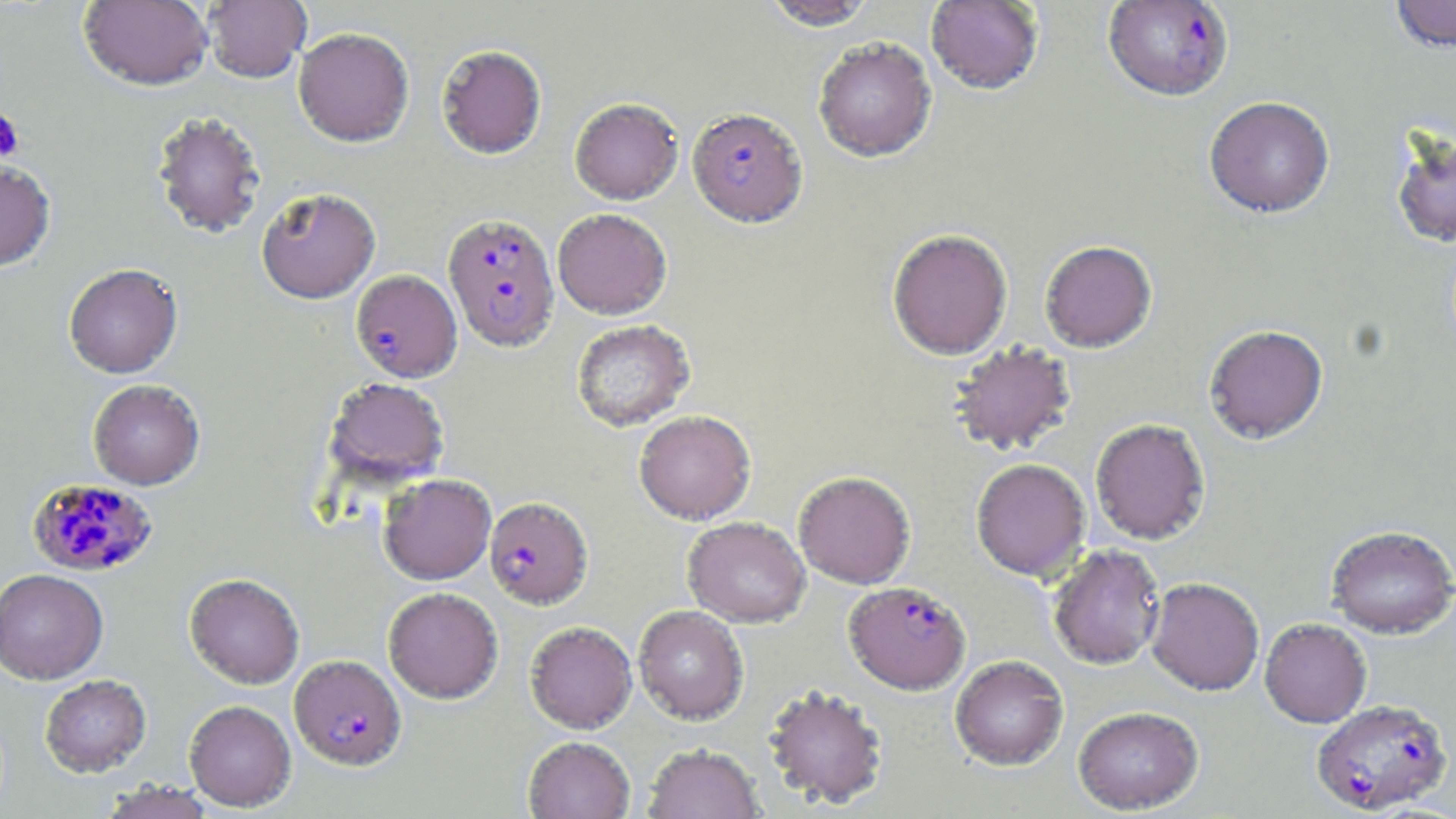

slide_level_diagnosis: Plasmodium falciparum
field_of_view: single
plasmodium_falciparum_infected_red_blood_cell_locations: 'approximate bounding boxes as named x1/y1/x2/y2 corners in pixels: (x1=1103, y1=1, x2=1234, y2=101), (x1=687, y1=107, x2=808, y2=227), (x1=443, y1=213, x2=559, y2=351), (x1=351, y1=269, x2=462, y2=382), (x1=24, y1=479, x2=155, y2=576), (x1=484, y1=496, x2=593, y2=608), (x1=844, y1=581, x2=970, y2=694), (x1=289, y1=654, x2=406, y2=770), (x1=1311, y1=698, x2=1453, y2=815)'
image_size: 1456×819 pixels
modality: light microscopy
stain: May-Grünwald-Giemsa
uninfected_red_blood_cell_locations: 'approximate bounding boxes as named x1/y1/x2/y2 corners in pixels: (x1=78, y1=0, x2=214, y2=90), (x1=203, y1=0, x2=311, y2=83), (x1=761, y1=0, x2=877, y2=30), (x1=1389, y1=0, x2=1456, y2=53), (x1=925, y1=1, x2=1045, y2=94), (x1=293, y1=27, x2=414, y2=147), (x1=813, y1=37, x2=937, y2=162), (x1=436, y1=44, x2=547, y2=159), (x1=1204, y1=96, x2=1335, y2=218), (x1=569, y1=97, x2=684, y2=204), (x1=150, y1=111, x2=267, y2=238), (x1=1389, y1=125, x2=1456, y2=248), (x1=0, y1=158, x2=56, y2=271), (x1=256, y1=186, x2=380, y2=303), (x1=553, y1=208, x2=672, y2=319), (x1=887, y1=228, x2=1013, y2=359), (x1=1039, y1=240, x2=1157, y2=352), (x1=63, y1=263, x2=183, y2=378), (x1=571, y1=319, x2=695, y2=431), (x1=1203, y1=324, x2=1328, y2=444), (x1=948, y1=341, x2=1078, y2=456), (x1=324, y1=377, x2=450, y2=487), (x1=88, y1=379, x2=205, y2=489), (x1=634, y1=409, x2=756, y2=524), (x1=1090, y1=418, x2=1211, y2=545), (x1=970, y1=458, x2=1091, y2=581), (x1=793, y1=471, x2=916, y2=588), (x1=378, y1=474, x2=496, y2=584), (x1=682, y1=516, x2=810, y2=628), (x1=1326, y1=525, x2=1456, y2=638), (x1=1047, y1=543, x2=1166, y2=670), (x1=0, y1=569, x2=108, y2=684), (x1=185, y1=573, x2=304, y2=689), (x1=1146, y1=577, x2=1265, y2=695), (x1=383, y1=587, x2=503, y2=703), (x1=633, y1=605, x2=749, y2=724), (x1=1259, y1=617, x2=1372, y2=727), (x1=525, y1=621, x2=637, y2=733), (x1=950, y1=655, x2=1069, y2=770), (x1=40, y1=674, x2=151, y2=777), (x1=762, y1=683, x2=889, y2=810), (x1=184, y1=699, x2=296, y2=811), (x1=1073, y1=705, x2=1204, y2=814), (x1=522, y1=736, x2=635, y2=819), (x1=642, y1=743, x2=764, y2=818), (x1=99, y1=780, x2=217, y2=819)'
platelet_locations: 'approximate bounding boxes as named x1/y1/x2/y2 corners in pixels: (x1=0, y1=107, x2=25, y2=162)'
magnification: 1000x
preparation: thin blood film